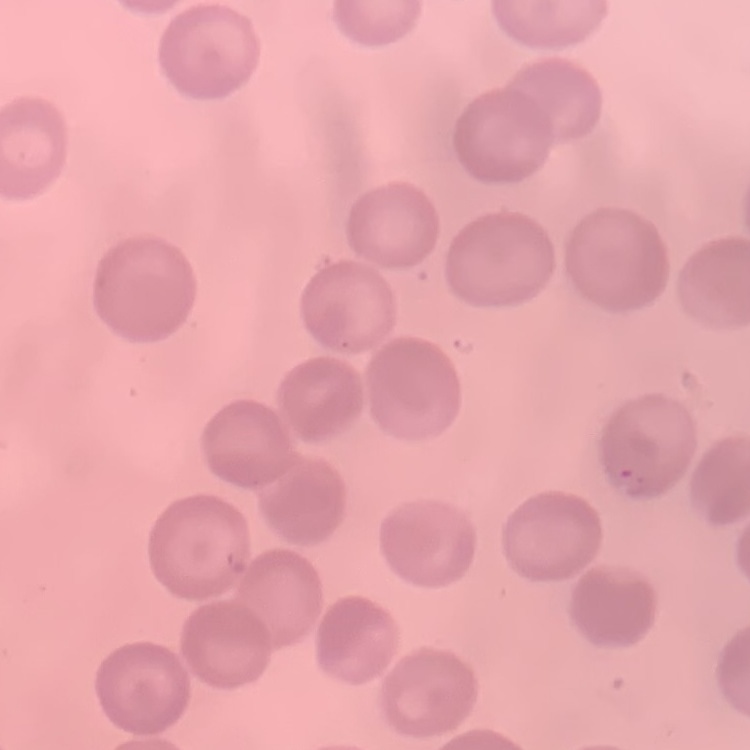

{
  "red_blood_cell_morphology": "no rouleaux formation",
  "image_type": "one tile cut from a larger photomicrograph",
  "preparation": "thin blood smear",
  "stain": "Field's or Giemsa"
}